Locate and identify every blood parasite.
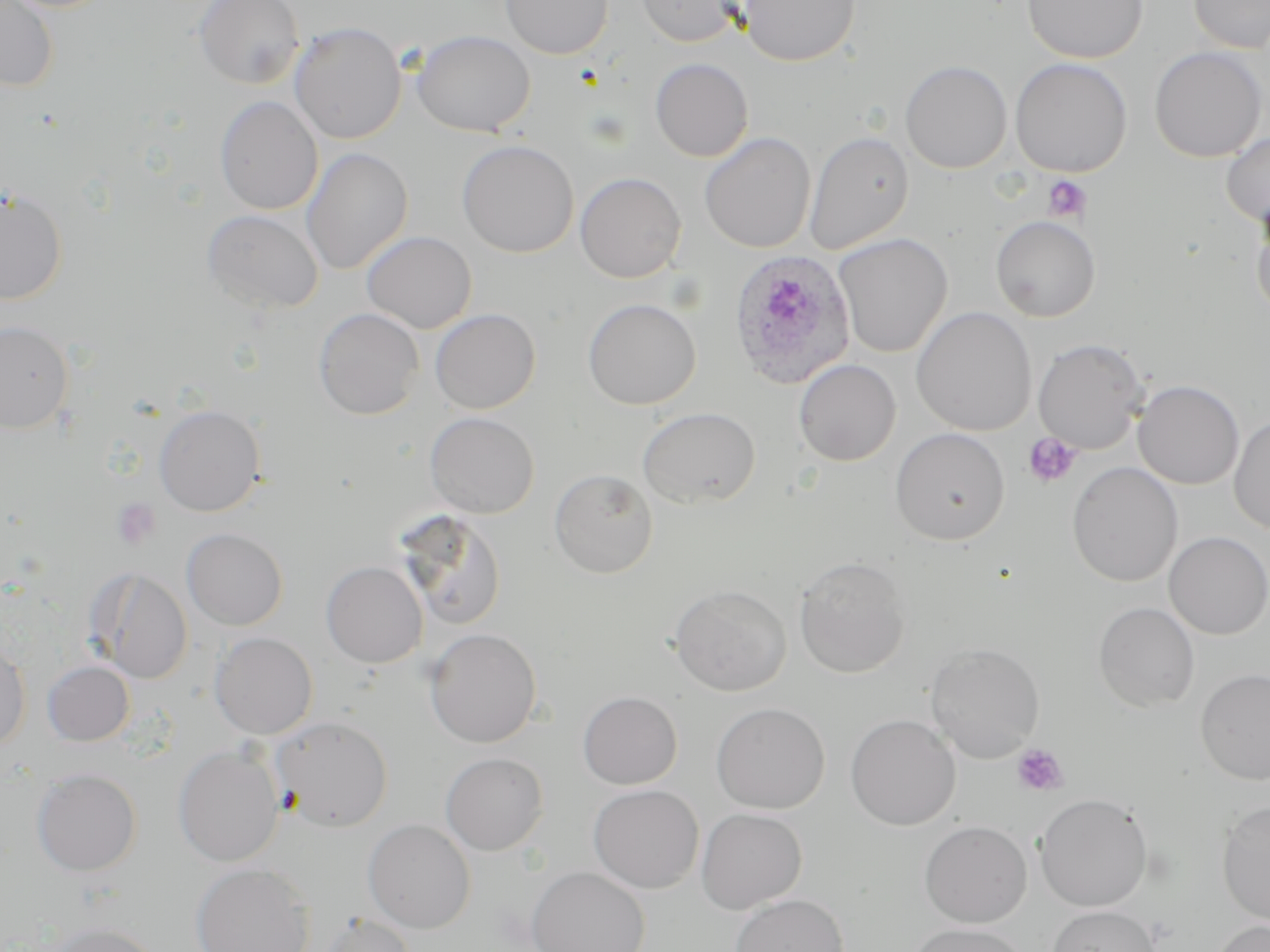

Approximate bounding boxes as [x1, y1, x2, y2] in pixels.
Plasmodium ovale-infected red blood cells: [727, 249, 858, 390].
No Plasmodium falciparum, Plasmodium malariae, Plasmodium vivax, Babesia divergens, or Trypanosoma brucei observed.

slide_level_diagnosis: Plasmodium ovale
uninfected_red_blood_cell_locations: 'approximate bounding boxes as [x1, y1, x2, y2] in pixels: [0, 0, 60, 92], [194, 0, 305, 89], [501, 0, 613, 59], [636, 0, 742, 46], [738, 0, 860, 66], [1023, 0, 1148, 63], [1188, 0, 1270, 53], [289, 21, 407, 144], [412, 29, 535, 137], [1149, 47, 1267, 162], [650, 58, 754, 162], [1010, 58, 1132, 177], [900, 60, 1012, 173], [215, 96, 323, 215], [804, 131, 914, 255], [1221, 131, 1270, 228], [699, 132, 816, 252], [456, 139, 579, 257], [301, 146, 413, 275], [575, 172, 686, 282], [0, 188, 68, 304], [1251, 206, 1270, 320], [202, 209, 324, 315], [991, 215, 1100, 322], [361, 230, 477, 333], [833, 233, 953, 358], [582, 298, 701, 410], [911, 306, 1037, 436], [314, 307, 424, 419], [430, 308, 540, 414], [0, 320, 73, 434], [1033, 338, 1148, 454], [794, 359, 901, 466], [1133, 380, 1244, 489], [154, 405, 265, 516], [637, 407, 761, 509], [425, 412, 540, 518], [1229, 414, 1270, 535], [890, 427, 1010, 545], [1067, 461, 1183, 587], [549, 469, 658, 579], [395, 510, 509, 632], [181, 528, 288, 630], [1164, 531, 1270, 639], [794, 555, 912, 678], [321, 560, 428, 668], [89, 568, 194, 684], [669, 584, 792, 696], [1093, 602, 1200, 712], [424, 628, 543, 748], [210, 632, 318, 739], [0, 637, 31, 753], [925, 643, 1045, 762], [42, 661, 135, 745], [1196, 669, 1270, 785], [577, 691, 682, 789], [711, 702, 830, 814], [845, 714, 961, 830], [271, 715, 393, 831], [173, 745, 284, 866], [440, 752, 549, 855], [32, 768, 142, 875], [588, 784, 704, 893], [1034, 793, 1153, 912], [1216, 800, 1270, 925], [696, 808, 808, 914], [363, 818, 476, 933], [919, 820, 1032, 927], [190, 862, 315, 952], [525, 867, 650, 952], [730, 894, 849, 952], [1047, 905, 1161, 952], [318, 913, 417, 952], [1209, 920, 1270, 952], [44, 921, 164, 952], [906, 923, 1031, 951]'
image_size: 1270×952 pixels
platelet_locations: 'approximate bounding boxes as [x1, y1, x2, y2] in pixels: [1042, 174, 1091, 223], [1022, 432, 1082, 489], [111, 498, 162, 550], [1012, 743, 1069, 797]'
field_of_view: one of a larger specimen
modality: optical microscopy
stain: May-Grünwald-Giemsa
preparation: thin blood smear
magnification: 1000x